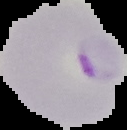

Summary:
  - Image type: segmented cell region with the area outside set to black
  - Preparation: thin blood film
  - Image size: 127×130 pixels
  - Malaria status: parasitized